Identify the preparation type.
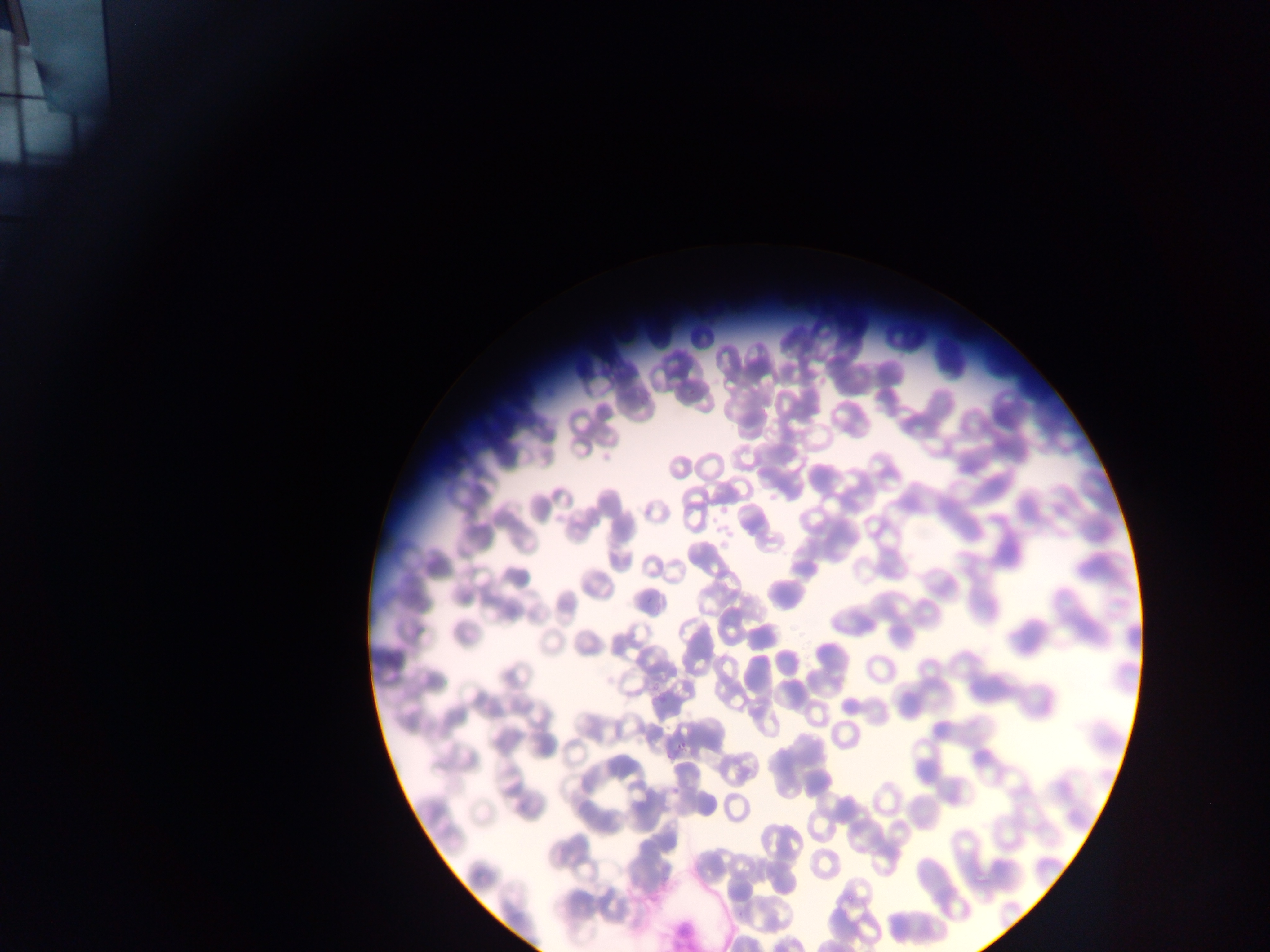

Thin blood film.

Approximate bounding boxes as left top right bottom in pixels. Malaria parasite locations: 596 445 618 467; 718 503 731 514; 710 511 720 525; 707 520 725 538; 711 533 729 556; 679 739 687 750; 665 751 675 762; 670 788 678 798. Image is 1270×952 pixels. Mobile-phone photograph taken through the microscope. One field of view. Sample from Ghana.